Assess this cell for malaria.
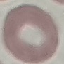
It is uninfected.

Acquired by smartphone through the microscope eyepiece. Thin blood film. Giemsa-stained preparation. Automatically extracted cell patch, resized to 64 × 64 pixels.